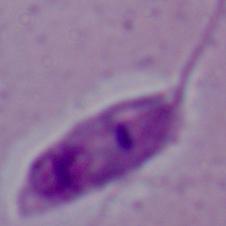

A Leishmania parasite is seen. 1000x magnification. Photomicrograph.